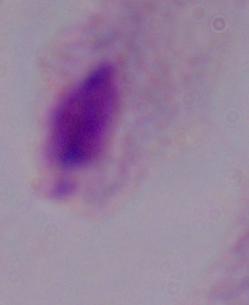

modality: photomicrograph
identification: trichomonad
magnification: 1000x